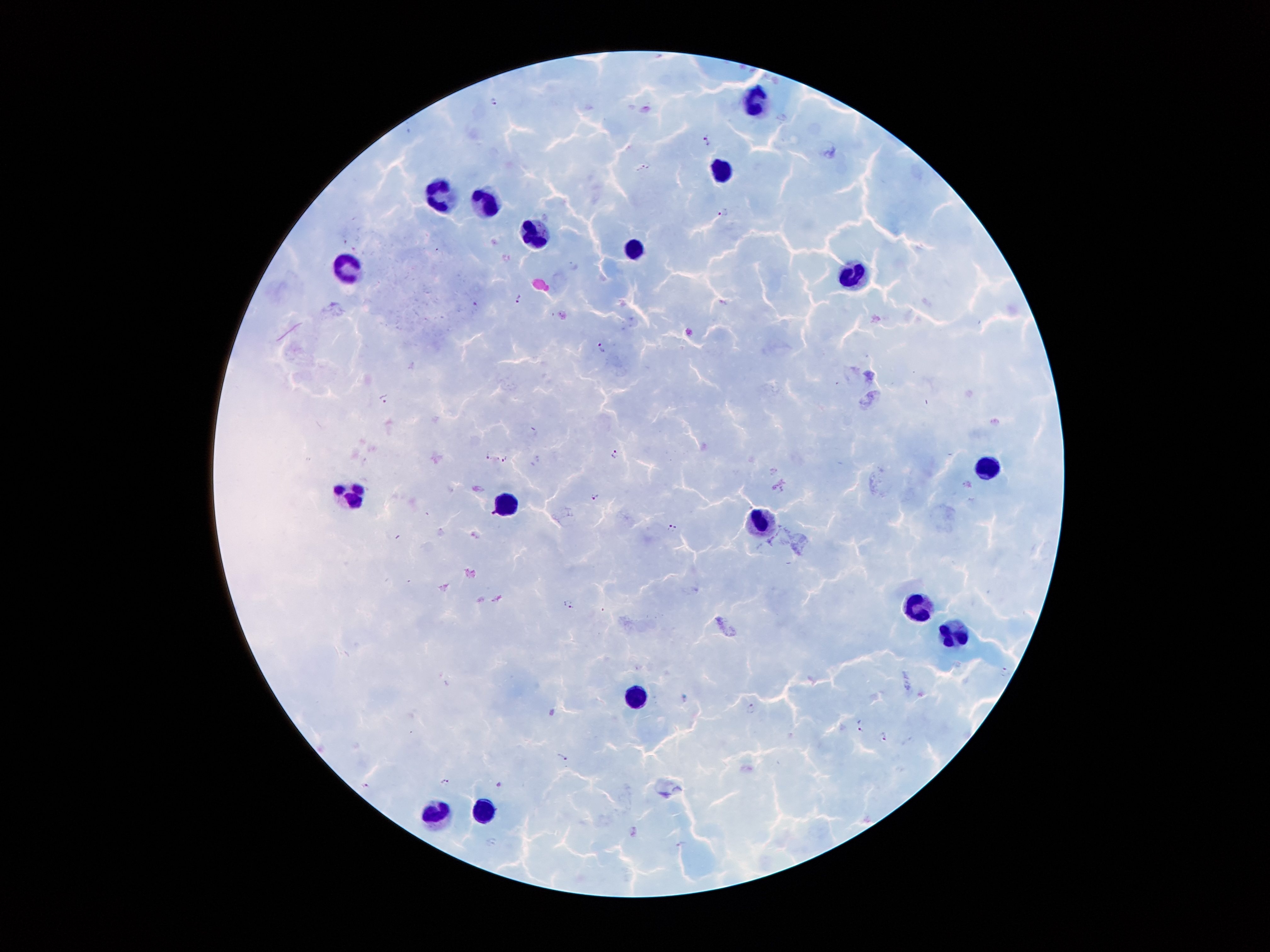
Approximate centers as [x, y] in pixels.
Summary:
  - Leukocyte locations: [750, 99], [721, 169], [439, 193], [490, 202], [534, 232], [637, 250], [349, 267], [848, 275], [991, 467], [350, 498], [506, 505], [759, 522], [916, 609], [958, 633], [637, 696], [482, 810], [437, 814]
  - Plasmodium parasite locations: [495, 101], [707, 139], [646, 164], [724, 210], [519, 297], [725, 301], [478, 305], [601, 347], [385, 398], [489, 455], [615, 456], [504, 458], [594, 496], [673, 527], [570, 603], [1005, 672], [752, 707], [861, 725], [884, 736], [564, 757], [446, 782], [365, 785], [499, 785]
  - Capture: smartphone camera through the microscope eyepiece
  - Magnification: 100x
  - Patient malaria status: positive for Plasmodium falciparum
  - Image size: 1270×952 pixels
  - Preparation: thick blood smear
  - Stain: Giemsa
  - Field of view: single